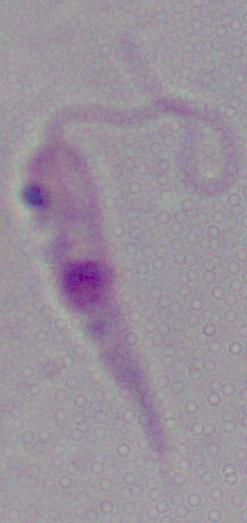

Micrograph. Captured at 1000x magnification. A Leishmania parasite is shown.